Identify the blood parasite species.
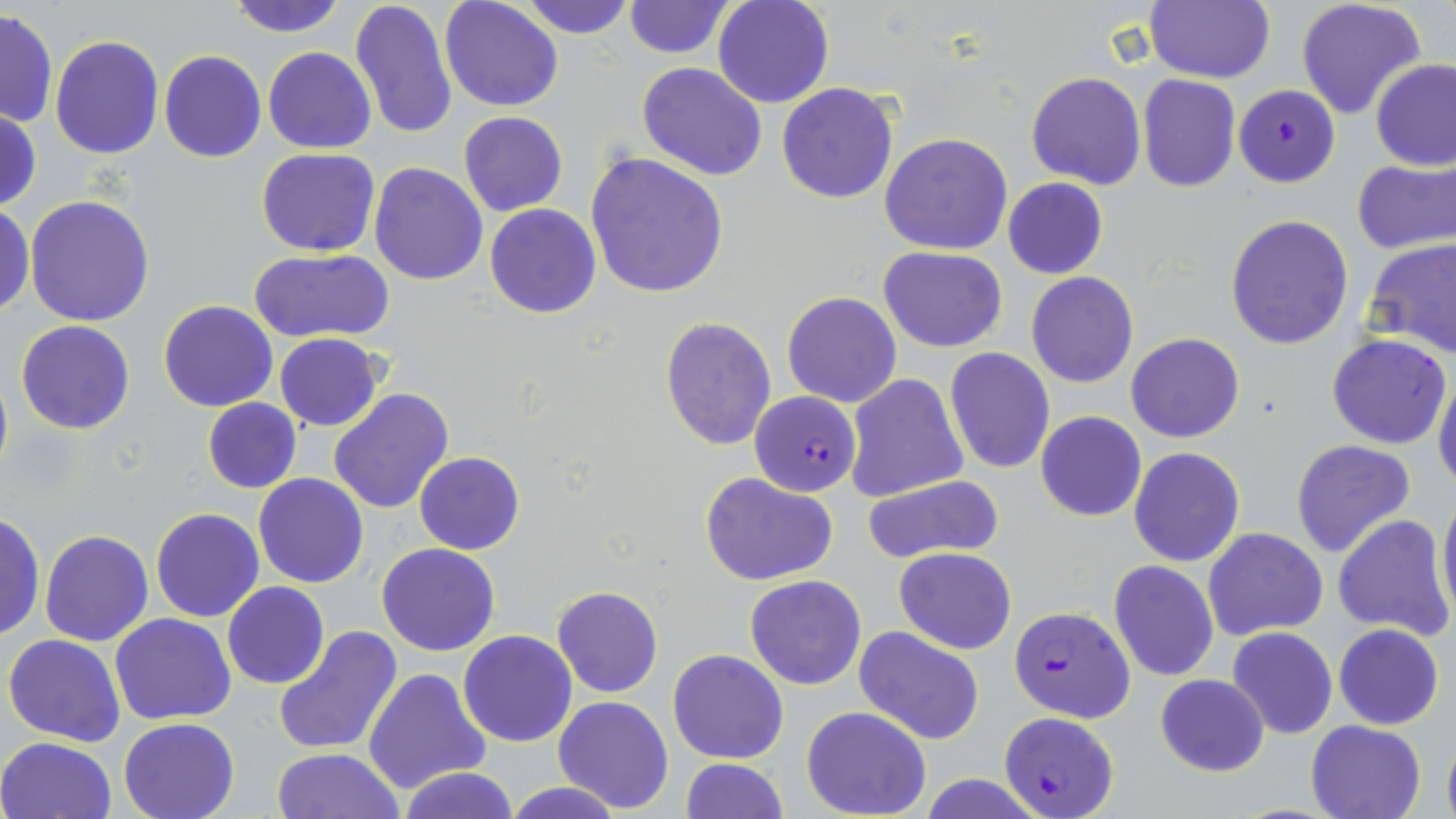
Plasmodium falciparum.

magnification: 1000x
plasmodium_falciparum_infected_red_blood_cell_locations: 'approximate bounding boxes as [x1, y1, x2, y2] in pixels: [1234, 84, 1340, 187], [751, 391, 860, 496], [1011, 606, 1137, 722], [998, 710, 1120, 819]'
uninfected_red_blood_cell_locations: 'approximate bounding boxes as [x1, y1, x2, y2] in pixels: [225, 0, 348, 35], [350, 0, 458, 143], [439, 0, 564, 112], [518, 0, 637, 38], [622, 0, 733, 58], [713, 0, 834, 108], [1146, 0, 1275, 84], [1295, 0, 1428, 120], [1, 9, 57, 129], [49, 33, 162, 158], [264, 46, 376, 153], [159, 50, 267, 163], [1371, 58, 1455, 172], [637, 62, 767, 182], [1026, 71, 1146, 190], [1137, 75, 1240, 192], [777, 82, 899, 203], [1, 108, 41, 211], [459, 111, 567, 216], [880, 132, 1013, 255], [257, 147, 380, 256], [585, 152, 729, 299], [1352, 157, 1455, 256], [370, 162, 488, 285], [1003, 178, 1109, 277], [25, 194, 156, 326], [0, 200, 34, 318], [485, 204, 600, 319], [1225, 214, 1354, 349], [1363, 237, 1456, 357], [879, 246, 1006, 351], [248, 249, 395, 343], [1025, 272, 1139, 388], [782, 291, 901, 408], [158, 299, 278, 413], [659, 317, 776, 449], [16, 320, 135, 435], [1126, 332, 1244, 443], [274, 333, 384, 432], [1326, 334, 1453, 449], [945, 347, 1055, 473], [0, 364, 13, 488], [1434, 369, 1456, 492], [845, 374, 968, 503], [328, 388, 455, 515], [203, 397, 301, 493], [1035, 411, 1145, 522], [1291, 439, 1416, 557], [1129, 446, 1245, 566], [414, 452, 525, 554], [253, 474, 370, 588], [700, 474, 840, 586], [863, 475, 1004, 563], [1437, 488, 1456, 625], [151, 507, 263, 621], [0, 512, 45, 644], [1332, 515, 1453, 640], [1203, 527, 1328, 639], [40, 529, 153, 647], [377, 543, 501, 656], [894, 546, 1017, 654], [1108, 560, 1219, 682], [745, 574, 867, 690], [222, 581, 330, 688], [551, 586, 663, 698], [111, 613, 236, 725], [1333, 624, 1443, 730], [273, 625, 403, 756], [854, 627, 985, 748], [1226, 627, 1338, 740], [458, 630, 577, 747], [4, 633, 126, 747], [667, 648, 790, 764], [364, 667, 492, 795], [1155, 672, 1270, 777], [552, 696, 674, 812], [801, 706, 932, 819], [117, 717, 239, 819], [1306, 719, 1426, 819], [1441, 731, 1456, 819], [0, 736, 117, 819], [271, 747, 403, 819], [680, 757, 786, 818], [395, 767, 520, 818], [916, 775, 1048, 819], [501, 780, 626, 818]'
image_size: 1456×819 pixels
preparation: thin blood film
modality: optical microscopy
stain: May-Grünwald-Giemsa
field_of_view: single